Identify the blood parasite species.
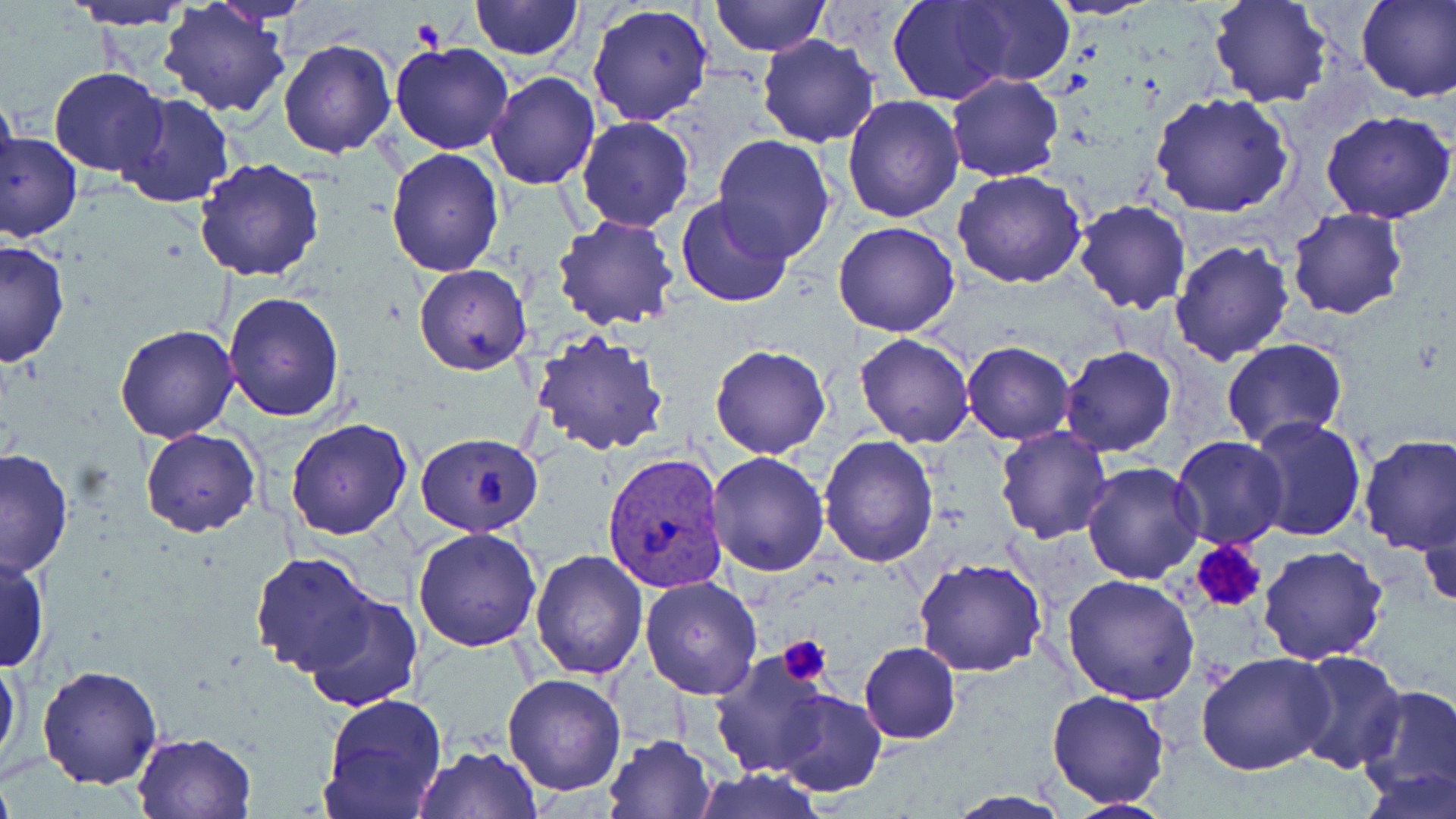
Plasmodium vivax.

Approximate bounding boxes as named x1/y1/x2/y2 corners in pixels. Plasmodium vivax-infected red blood cell locations: (x1=603, y1=453, x2=732, y2=595). Uninfected red blood cell locations: (x1=63, y1=0, x2=193, y2=29), (x1=469, y1=0, x2=584, y2=59), (x1=949, y1=0, x2=1076, y2=87), (x1=1047, y1=0, x2=1160, y2=21), (x1=1356, y1=0, x2=1456, y2=102), (x1=708, y1=1, x2=832, y2=57), (x1=888, y1=1, x2=1020, y2=105), (x1=1210, y1=1, x2=1332, y2=109), (x1=159, y1=3, x2=292, y2=118), (x1=586, y1=5, x2=715, y2=126), (x1=758, y1=35, x2=881, y2=148), (x1=278, y1=38, x2=396, y2=157), (x1=389, y1=40, x2=515, y2=154), (x1=48, y1=67, x2=168, y2=176), (x1=485, y1=72, x2=599, y2=189), (x1=946, y1=73, x2=1064, y2=182), (x1=0, y1=86, x2=19, y2=193), (x1=1149, y1=91, x2=1295, y2=218), (x1=113, y1=93, x2=235, y2=208), (x1=843, y1=96, x2=964, y2=223), (x1=1322, y1=111, x2=1456, y2=224), (x1=576, y1=115, x2=695, y2=233), (x1=1, y1=130, x2=82, y2=242), (x1=713, y1=134, x2=837, y2=261), (x1=386, y1=149, x2=504, y2=278), (x1=194, y1=156, x2=326, y2=281), (x1=952, y1=168, x2=1088, y2=288), (x1=674, y1=197, x2=795, y2=308), (x1=1073, y1=199, x2=1192, y2=314), (x1=1287, y1=208, x2=1408, y2=320), (x1=552, y1=216, x2=679, y2=331), (x1=832, y1=220, x2=960, y2=338), (x1=0, y1=239, x2=70, y2=369), (x1=1169, y1=240, x2=1294, y2=364), (x1=414, y1=263, x2=533, y2=375), (x1=223, y1=292, x2=346, y2=423), (x1=114, y1=323, x2=238, y2=443), (x1=531, y1=329, x2=672, y2=458), (x1=855, y1=333, x2=975, y2=448), (x1=1221, y1=339, x2=1348, y2=451), (x1=961, y1=341, x2=1074, y2=445), (x1=709, y1=344, x2=831, y2=459), (x1=1060, y1=345, x2=1178, y2=458), (x1=1245, y1=414, x2=1366, y2=540), (x1=285, y1=417, x2=413, y2=540), (x1=994, y1=426, x2=1113, y2=544), (x1=139, y1=427, x2=260, y2=537), (x1=417, y1=432, x2=545, y2=537), (x1=1357, y1=434, x2=1456, y2=555), (x1=820, y1=435, x2=938, y2=568), (x1=1171, y1=435, x2=1288, y2=551), (x1=0, y1=446, x2=75, y2=580), (x1=706, y1=451, x2=831, y2=576), (x1=1080, y1=462, x2=1205, y2=585), (x1=1419, y1=499, x2=1456, y2=615), (x1=412, y1=526, x2=543, y2=651), (x1=1260, y1=545, x2=1389, y2=664), (x1=0, y1=547, x2=49, y2=674), (x1=249, y1=551, x2=383, y2=675), (x1=530, y1=551, x2=648, y2=680), (x1=914, y1=558, x2=1047, y2=678), (x1=1062, y1=574, x2=1201, y2=704), (x1=640, y1=575, x2=763, y2=700), (x1=303, y1=592, x2=422, y2=713), (x1=859, y1=641, x2=961, y2=745), (x1=709, y1=647, x2=832, y2=780), (x1=1290, y1=649, x2=1407, y2=772), (x1=1195, y1=650, x2=1335, y2=776), (x1=0, y1=651, x2=22, y2=773), (x1=37, y1=664, x2=163, y2=790), (x1=502, y1=673, x2=626, y2=796), (x1=1356, y1=686, x2=1456, y2=805), (x1=1047, y1=689, x2=1171, y2=808), (x1=774, y1=690, x2=886, y2=796), (x1=319, y1=693, x2=448, y2=819), (x1=132, y1=731, x2=256, y2=818), (x1=603, y1=733, x2=718, y2=819), (x1=413, y1=745, x2=543, y2=819), (x1=1358, y1=766, x2=1454, y2=819), (x1=691, y1=768, x2=823, y2=819), (x1=944, y1=791, x2=1072, y2=819), (x1=1062, y1=799, x2=1174, y2=817). Platelet locations: (x1=408, y1=16, x2=447, y2=50), (x1=1190, y1=540, x2=1268, y2=614), (x1=779, y1=636, x2=831, y2=686). Thin blood smear. May-Grünwald-Giemsa-stained preparation. Captured at 1000x magnification. Image is 1456×819 pixels. Single field of view. Light microscopy.